Describe the morphology of the red blood cells.
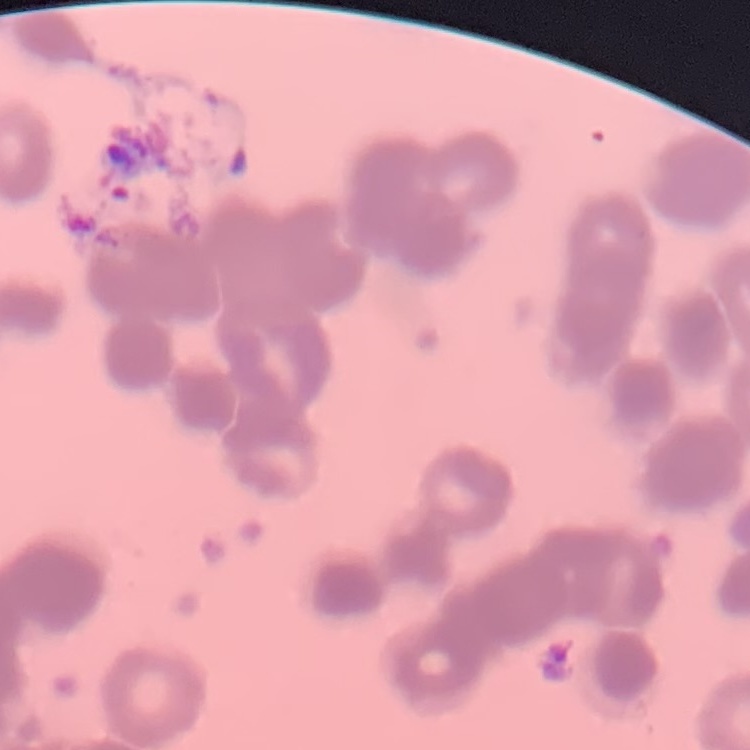
They show rouleaux formation.

Summary:
  - Stain: Field's or Giemsa
  - Preparation: thin blood smear
  - Image type: square crop of a larger photomicrograph